Classify this cell by malaria status.
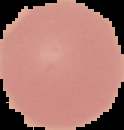
Uninfected.

image size = 124×130 pixels
image type = segmented cell region with the area outside set to black
preparation = thin blood film